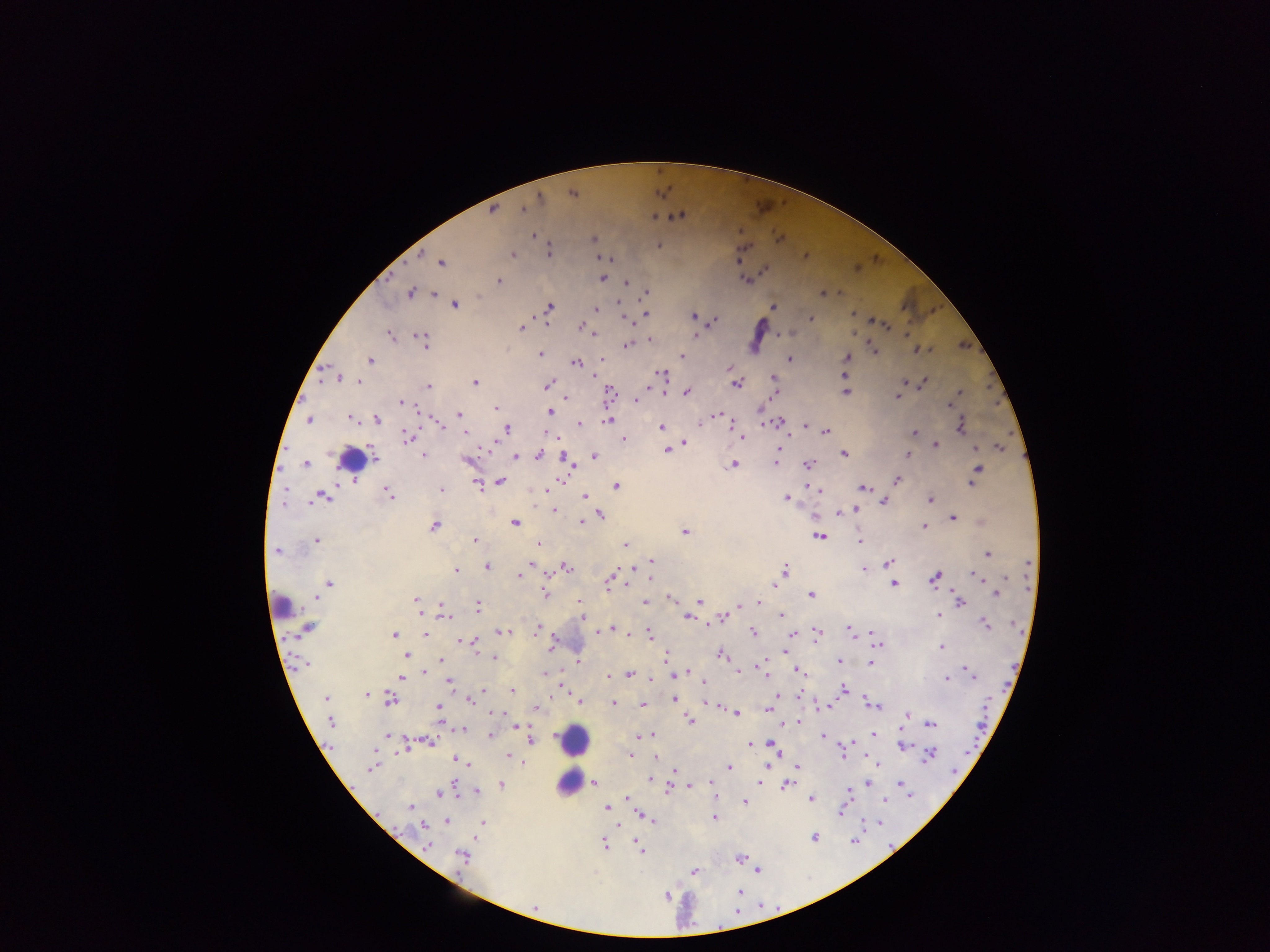

{
  "capture": "mobile-phone photograph through a microscope",
  "plasmodium_parasite_locations": "approximate centers as [x, y] in pixels: [572, 194], [537, 196], [493, 209], [522, 209], [654, 216], [678, 216], [533, 235], [778, 239], [593, 240], [659, 245], [548, 252], [512, 255], [739, 256], [804, 256], [604, 258], [610, 259], [441, 262], [764, 269], [602, 278], [747, 280], [497, 281], [624, 281], [645, 291], [837, 291], [410, 293], [433, 293], [822, 294], [455, 304], [773, 306], [550, 307], [596, 309], [852, 314], [646, 315], [693, 316], [810, 318], [627, 319], [712, 320], [547, 321], [871, 322], [881, 324], [886, 325], [520, 327], [581, 327], [908, 333], [389, 334], [594, 334], [779, 335], [694, 336], [649, 339], [423, 341], [627, 344], [917, 350], [874, 351], [539, 354], [681, 356], [846, 357], [369, 360], [601, 360], [789, 360], [576, 361], [730, 368], [661, 374], [844, 375], [336, 378], [773, 378], [921, 381], [360, 382], [474, 383], [736, 383], [548, 385], [427, 386], [686, 391], [844, 392], [959, 392], [774, 393], [609, 394], [898, 395], [635, 401], [400, 402], [949, 406], [495, 408], [550, 411], [419, 412], [718, 413], [458, 414], [351, 418], [762, 418], [378, 419], [309, 420], [608, 420], [700, 422], [777, 422], [577, 423], [440, 424], [805, 425], [960, 425], [810, 426], [662, 427], [505, 429], [825, 430], [463, 432], [545, 432], [914, 433], [741, 437], [407, 438], [557, 438], [622, 439], [685, 441], [934, 445], [999, 447], [781, 448], [974, 448], [666, 450], [843, 453], [908, 454], [539, 455], [374, 456], [423, 456], [515, 456], [593, 456], [467, 459], [775, 462], [808, 463], [734, 464], [305, 465], [572, 465], [976, 473], [561, 479], [897, 479], [974, 481], [350, 482], [499, 482], [477, 484], [616, 486], [808, 487], [861, 487], [284, 489], [543, 489], [818, 489], [441, 490], [388, 493], [324, 495], [584, 496], [318, 497], [786, 498], [930, 499], [883, 501], [282, 504], [553, 510], [855, 510], [837, 512], [601, 514], [952, 518], [581, 521], [981, 521], [514, 522], [434, 525], [923, 527], [684, 532], [819, 536], [316, 540], [474, 540], [860, 542], [537, 543], [624, 544], [275, 551], [986, 554], [650, 560], [888, 562], [1027, 563], [486, 566], [567, 567], [863, 567], [631, 568], [455, 571], [784, 571], [548, 572], [610, 574], [519, 575], [1006, 576], [977, 577], [935, 578], [649, 579], [775, 580], [330, 583], [628, 583], [893, 583], [607, 585], [545, 593], [995, 593], [811, 594], [315, 597], [670, 597], [416, 599], [700, 600], [579, 601], [958, 601], [645, 602], [759, 602], [748, 604], [740, 605], [441, 606], [477, 606], [444, 612], [939, 613], [780, 615], [581, 616], [686, 616], [722, 617], [711, 622], [1010, 623], [984, 624], [306, 629], [535, 629], [612, 629], [506, 630], [599, 630], [618, 630], [871, 631], [751, 632], [815, 632], [627, 633], [850, 633], [424, 634], [650, 634], [393, 635], [459, 640], [473, 641], [552, 643], [877, 643], [940, 646], [478, 650], [784, 651], [407, 654], [720, 654], [495, 656], [665, 658], [440, 661], [837, 661], [577, 662], [868, 662], [760, 664], [303, 665], [965, 669], [738, 670], [797, 670], [424, 671], [685, 671], [763, 672], [543, 673], [968, 673], [629, 674], [678, 675], [607, 676], [401, 678], [947, 679], [448, 681], [703, 683], [562, 685], [844, 688], [512, 691], [484, 692], [367, 694], [799, 694], [776, 697], [326, 698], [389, 699], [469, 699], [674, 700], [866, 700], [580, 701], [613, 702], [714, 704], [873, 704], [642, 705], [829, 706], [439, 709], [535, 709], [767, 710], [491, 712], [736, 713], [907, 715], [690, 719], [331, 720], [798, 722], [445, 724], [930, 724], [514, 726], [463, 729], [873, 734], [490, 735], [649, 735], [654, 735], [822, 735], [386, 736], [642, 736], [531, 740], [430, 742], [749, 743], [848, 744], [771, 745], [902, 746], [406, 747], [777, 753], [841, 753], [928, 755], [509, 756], [630, 756], [844, 756], [865, 756], [654, 757], [455, 759], [514, 759], [521, 763], [469, 764], [766, 765], [879, 765], [729, 766], [797, 766], [372, 767], [673, 772], [649, 779], [760, 780], [710, 782], [758, 782], [594, 783], [868, 783], [900, 783], [501, 784], [787, 785], [689, 786], [457, 789], [667, 789], [476, 790], [847, 791], [438, 794], [911, 796], [626, 798], [715, 799], [810, 799], [884, 799], [745, 802], [606, 807], [411, 808], [840, 811], [639, 815], [714, 818], [649, 819], [446, 820], [653, 820], [878, 821], [482, 823], [425, 826], [814, 836], [604, 844], [427, 845], [638, 846], [640, 850], [462, 856], [740, 857], [757, 870], [693, 871], [740, 891], [666, 896], [535, 907]",
  "preparation": "thick blood film",
  "leukocyte_locations": "approximate centers as [x, y] in pixels: [350, 459], [282, 606], [573, 741], [567, 782]",
  "field_of_view": "single",
  "image_size": "1270×952 pixels",
  "country": "Ghana"
}